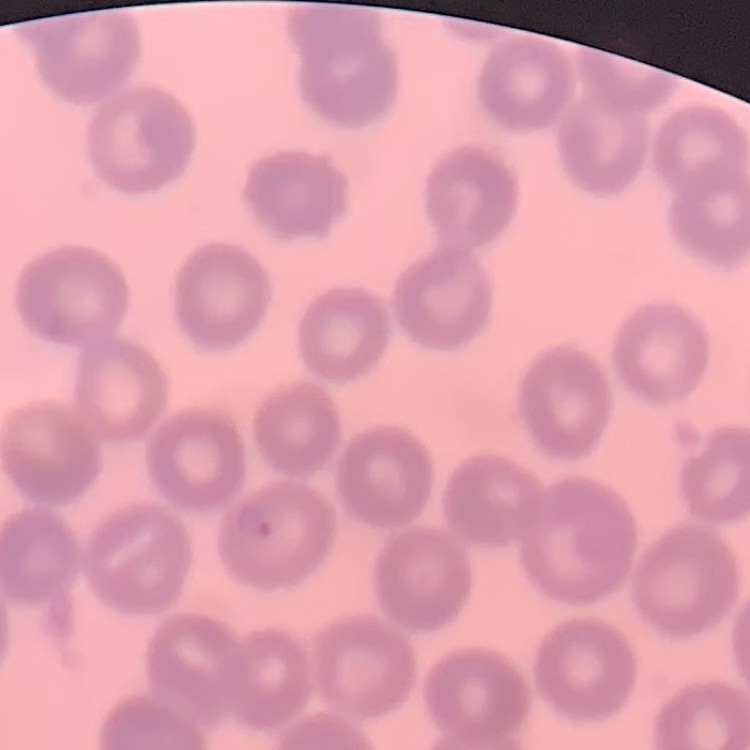

Summary:
  - Erythrocyte morphology: no rouleaux formation
  - Preparation: thin blood film
  - Image type: square crop of a larger photomicrograph
  - Stain: Field's or Giemsa